Name the parasite shown.
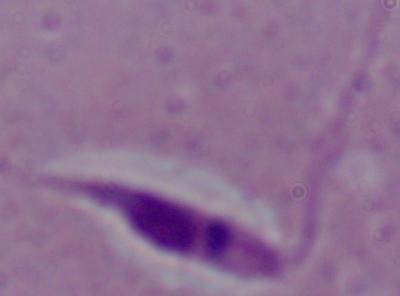

Leishmania.

Summary:
  - Modality: micrograph
  - Magnification: 1000x